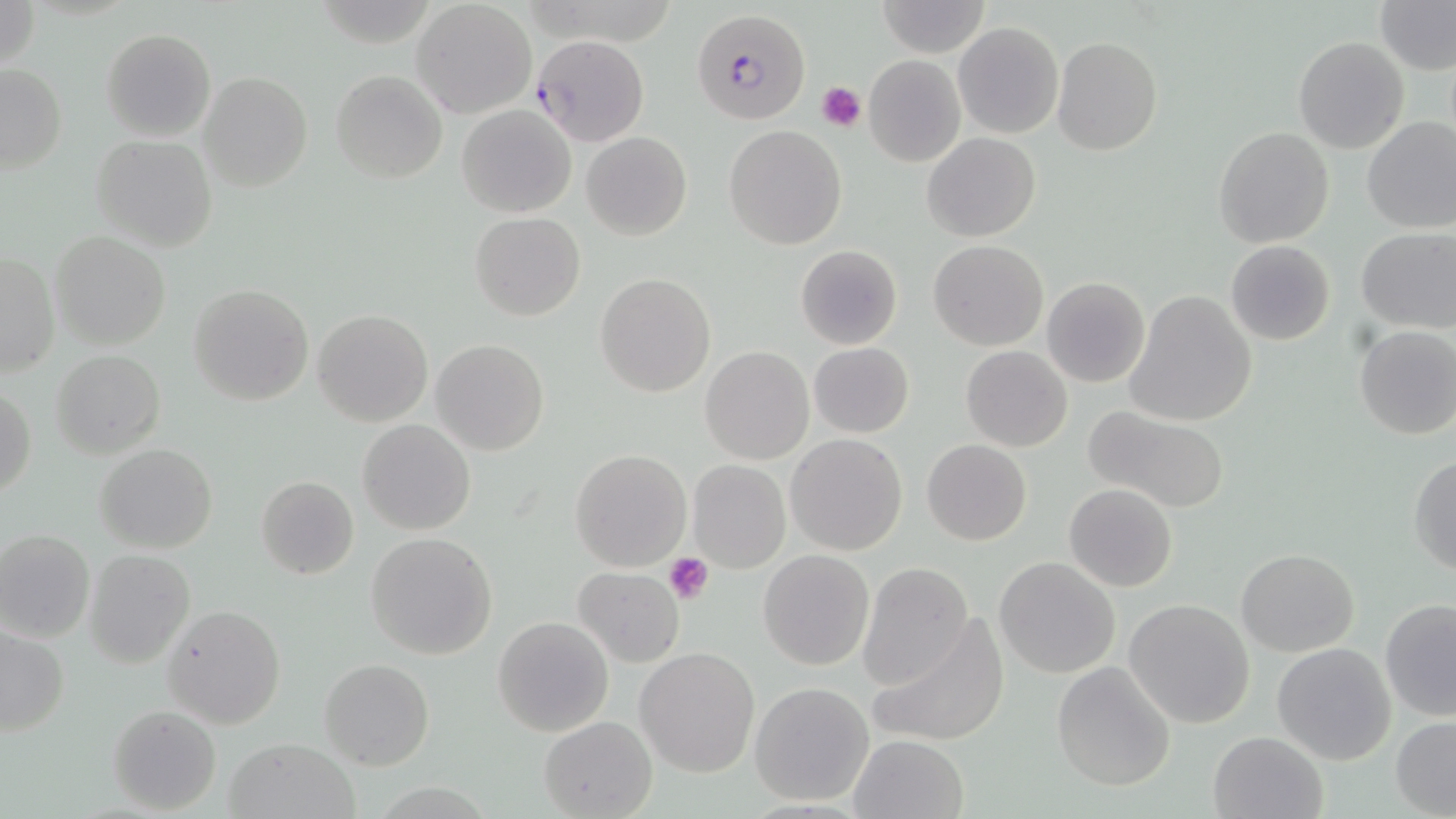

Summary:
  - Coordinate format: approximate bounding boxes as (x1,y1)-(x2,y2) corner pairs in pixels
  - Uninfected red blood cell locations: (1,0)-(42,73), (875,0)-(990,57), (412,1)-(537,118), (1378,1)-(1456,75), (953,22)-(1063,138), (100,28)-(216,142), (1051,36)-(1163,156), (1294,37)-(1408,155), (863,55)-(967,167), (0,63)-(66,171), (330,69)-(447,183), (198,71)-(313,192), (457,104)-(576,218), (1361,117)-(1456,235), (723,126)-(847,250), (1212,126)-(1335,249), (581,132)-(692,241), (922,133)-(1040,242), (90,134)-(217,252), (470,212)-(585,320), (1356,226)-(1455,333), (50,231)-(171,350), (929,239)-(1048,350), (1225,240)-(1336,345), (795,246)-(903,349), (1,250)-(59,379), (595,273)-(716,397), (1042,277)-(1151,389), (188,282)-(313,406), (1124,291)-(1258,427), (312,309)-(432,425), (1354,325)-(1456,440), (431,339)-(549,456), (809,342)-(913,438), (960,345)-(1073,453), (701,346)-(814,465), (51,349)-(166,460), (0,382)-(36,498), (1081,405)-(1230,514), (358,420)-(475,535), (785,434)-(908,555), (921,438)-(1032,545), (95,443)-(217,552), (570,449)-(690,570), (1408,453)-(1456,576), (688,460)-(789,572), (255,475)-(360,580), (1064,483)-(1179,592), (0,529)-(96,643), (366,532)-(498,660), (1236,548)-(1359,657), (84,549)-(194,667), (759,549)-(875,671), (994,556)-(1122,679), (856,562)-(974,688), (573,565)-(684,666), (1124,598)-(1256,729), (1379,598)-(1456,721), (163,604)-(286,729), (491,616)-(614,736), (865,617)-(1010,748), (1,626)-(70,738), (1270,642)-(1397,766), (636,646)-(760,777), (319,658)-(434,770), (1052,661)-(1177,791), (750,682)-(873,805), (107,704)-(223,815), (1390,715)-(1456,817), (539,716)-(657,818), (1208,732)-(1328,819), (848,733)-(969,819), (225,736)-(360,819)
  - Plasmodium falciparum-infected red blood cell locations: (692,9)-(810,125), (533,38)-(648,147)
  - Platelet locations: (816,81)-(866,131), (663,552)-(713,604)
  - Slide-level diagnosis: Plasmodium falciparum
  - Field of view: single
  - Preparation: thin blood smear
  - Stain: May-Grünwald-Giemsa
  - Magnification: 1000x
  - Image size: 1456×819 pixels
  - Modality: optical microscopy